Assess the morphology of the erythrocytes.
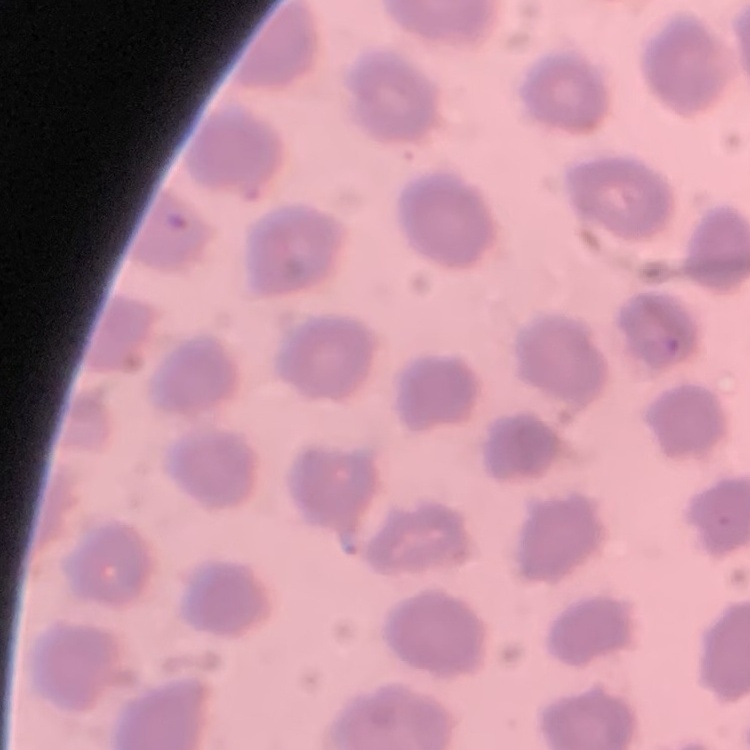

They show no rouleaux formation.

Summary:
  - Preparation: thin blood film
  - Stain: Field's or Giemsa
  - Image type: square crop of a larger photomicrograph